Locate Plasmodium parasites and leukocytes.
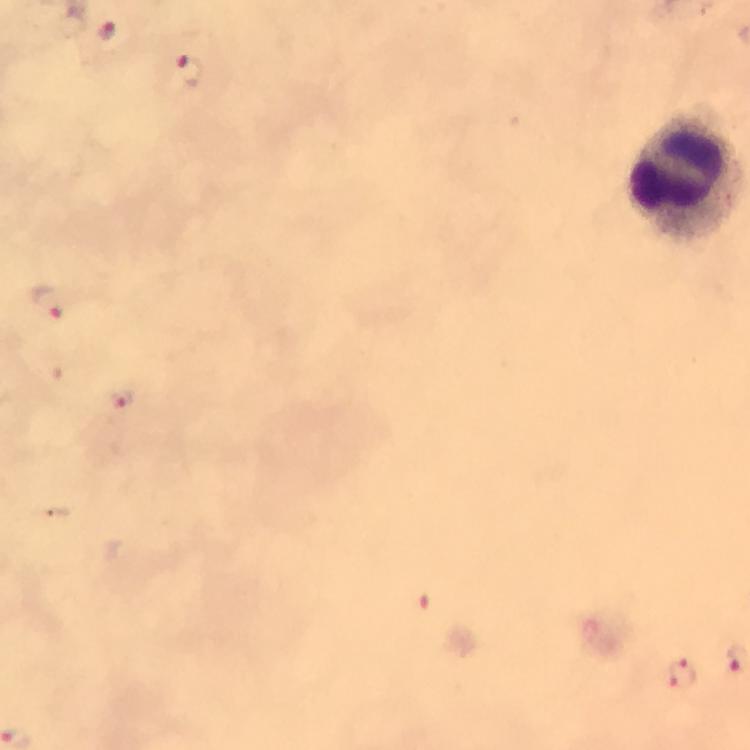
Approximate object centers, in pixels from the top-left corner.
Plasmodium parasites: (x=108, y=31), (x=188, y=70), (x=46, y=303), (x=121, y=397), (x=683, y=677).
Leukocytes: (x=686, y=178).

Summary:
  - Preparation: thick smear
  - Context: from a diagnostic examination for malaria
  - Image size: 750×750 pixels
  - Immersion oil: used
  - Cropped from: one field of view
  - Capture: smartphone mounted on the microscope
  - Stain: Giemsa
  - Magnification: 100x